Point out each Plasmodium parasite.
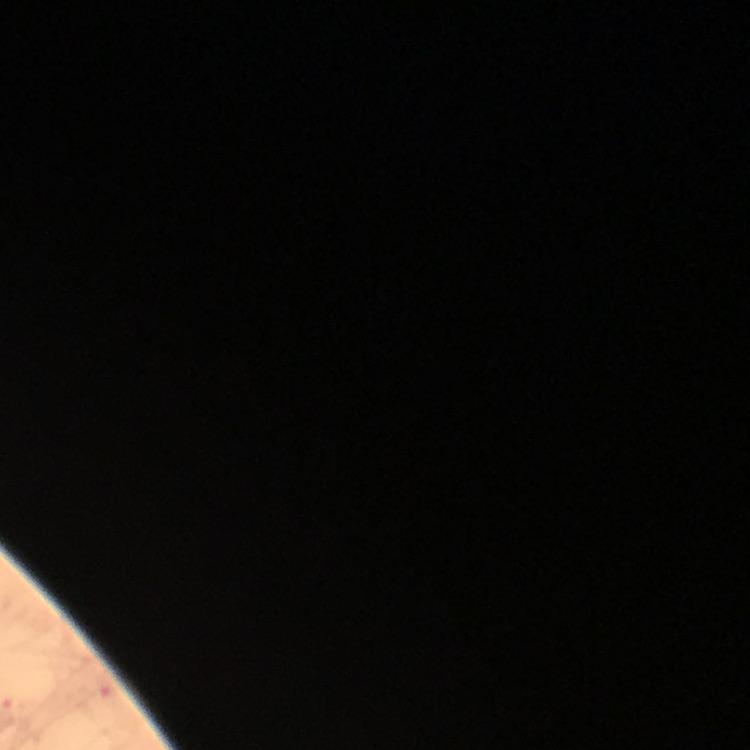

Approximate centers as {x, y} in pixels.
Plasmodium parasites: {107, 688}.

100x magnification. Immersion oil was used. Photographed through the microscope with a smartphone camera. Image is 750×750 pixels. Giemsa stain. Thick blood film. Cropped region of a single field of view. From a malaria diagnostic workup.